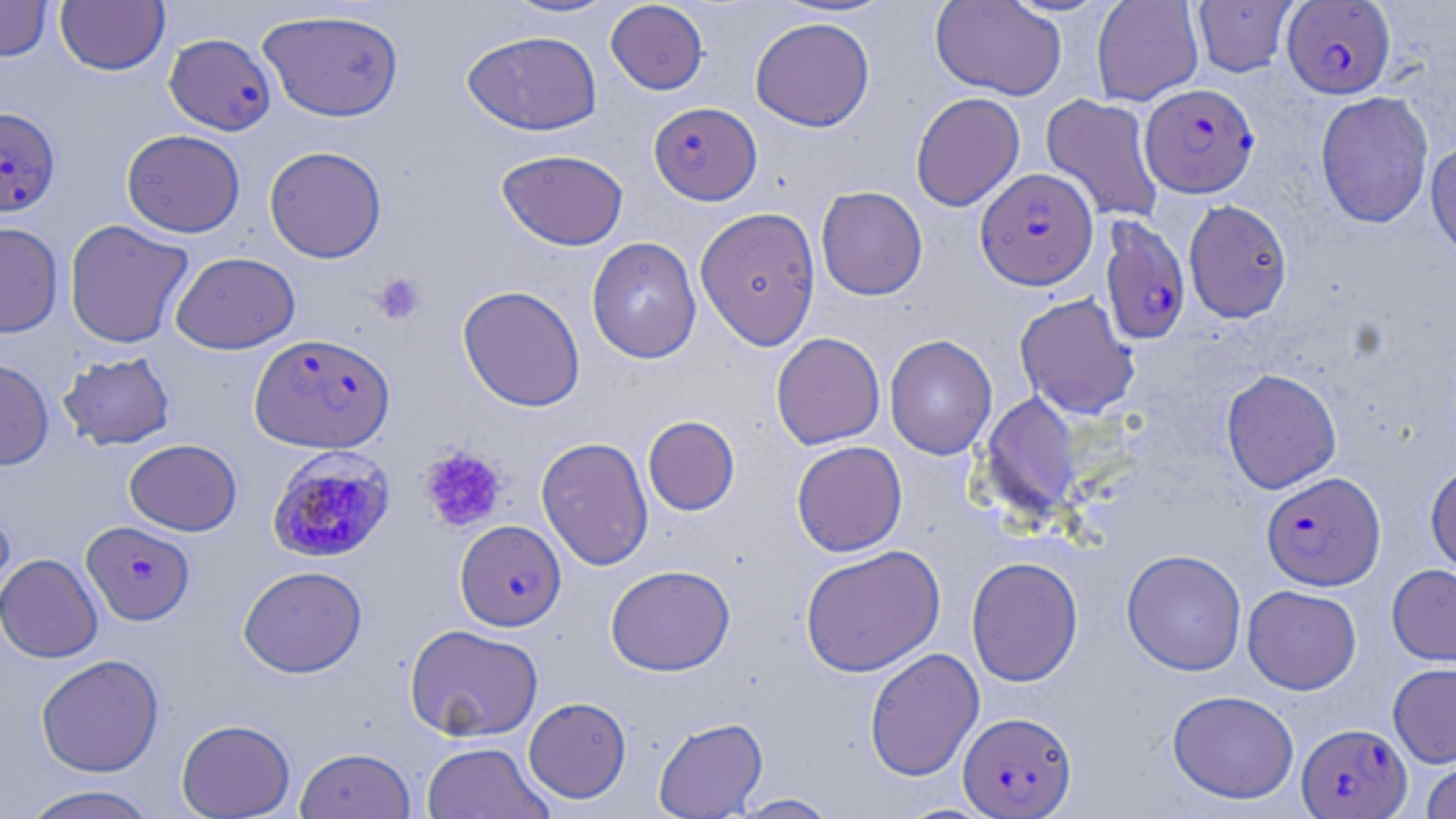
{
  "plasmodium_falciparum_infected_red_blood_cell_locations": "approximate bounding boxes as (x1, y1, x2, y2) in pixels: (1282, 1, 1396, 98), (164, 33, 276, 134), (1141, 83, 1259, 197), (648, 101, 762, 205), (0, 106, 61, 217), (975, 168, 1098, 289), (1100, 215, 1192, 346), (249, 333, 395, 453), (266, 446, 397, 564), (1261, 471, 1385, 590), (82, 520, 196, 626), (455, 520, 566, 631), (958, 711, 1077, 817), (1297, 723, 1412, 818)",
  "slide_level_diagnosis": "Plasmodium falciparum",
  "preparation": "thin blood film",
  "field_of_view": "single",
  "stain": "May-Grünwald-Giemsa",
  "platelet_locations": "approximate bounding boxes as (x1, y1, x2, y2) in pixels: (372, 272, 427, 325), (418, 445, 507, 534)",
  "uninfected_red_blood_cell_locations": "approximate bounding boxes as (x1, y1, x2, y2) in pixels: (498, 0, 621, 19), (930, 0, 1067, 99), (1091, 0, 1204, 105), (0, 1, 53, 61), (55, 1, 170, 75), (605, 1, 709, 95), (1192, 1, 1298, 77), (258, 9, 404, 122), (750, 18, 875, 131), (462, 30, 602, 136), (1315, 91, 1434, 229), (911, 92, 1025, 211), (1041, 94, 1164, 222), (122, 129, 246, 237), (1425, 137, 1456, 262), (264, 145, 387, 263), (496, 149, 629, 250), (816, 186, 927, 300), (1184, 199, 1292, 322), (695, 206, 822, 350), (64, 219, 194, 349), (0, 222, 64, 338), (586, 236, 702, 363), (170, 252, 300, 354), (458, 285, 586, 412), (1014, 293, 1140, 419), (771, 332, 886, 450), (884, 335, 997, 460), (58, 352, 175, 450), (0, 358, 54, 470), (1221, 369, 1342, 493), (980, 392, 1083, 521), (642, 415, 740, 516), (535, 436, 654, 571), (123, 438, 242, 536), (791, 441, 907, 556), (1426, 463, 1456, 578), (0, 506, 16, 618), (799, 545, 945, 677), (1122, 549, 1247, 675), (0, 553, 103, 663), (966, 556, 1084, 687), (1386, 563, 1456, 668), (605, 564, 735, 676), (238, 565, 368, 678), (1242, 585, 1361, 694), (404, 623, 543, 741), (864, 647, 984, 781), (36, 654, 164, 777), (1388, 662, 1456, 767), (1167, 690, 1299, 804), (523, 696, 632, 803), (652, 717, 768, 818), (176, 718, 296, 818), (420, 741, 555, 819), (295, 746, 417, 819), (1420, 760, 1456, 819), (18, 784, 163, 819), (730, 792, 842, 818)",
  "modality": "optical microscopy",
  "image_size": "1456×819 pixels",
  "magnification": "1000x"
}